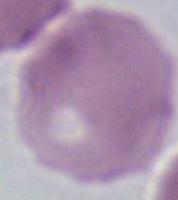
identification = red blood cell
modality = micrograph
magnification = 1000x